Report the malaria status of this cell.
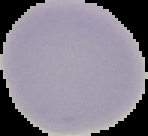

It is uninfected.

{
  "preparation": "thin blood smear",
  "image_size": "148×136 pixels",
  "image_type": "cell region segmented out of the field of view; surrounding area masked to black"
}